Describe the morphology of the red blood cells.
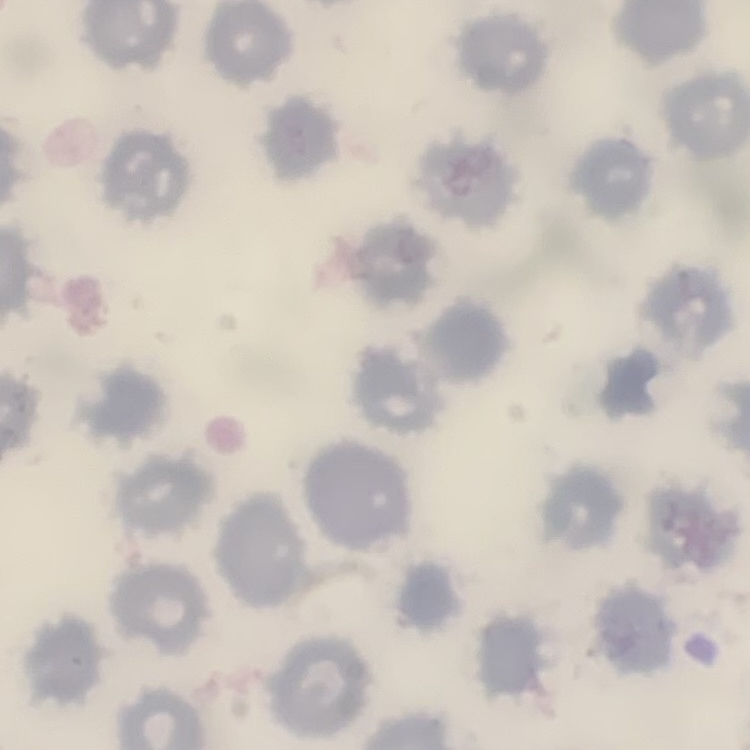
No rouleaux formation.

One tile cut from a larger photomicrograph. Thin blood film. Stained with either Field's or Giemsa.